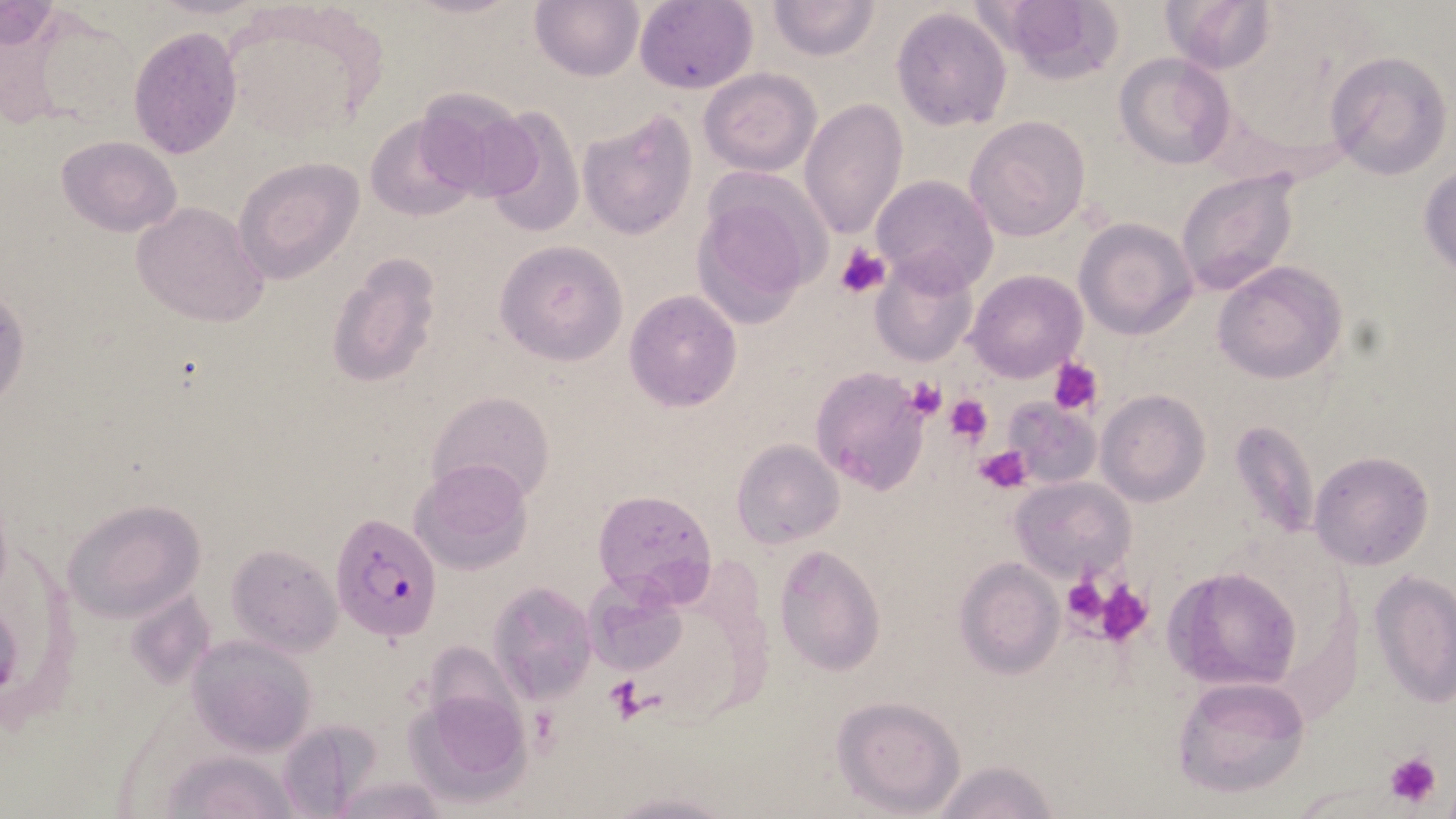
slide-level diagnosis = Plasmodium falciparum
stain = May-Grünwald-Giemsa
magnification = 1000x
modality = light microscopy
platelet locations = approximate bounding boxes as named x1/y1/x2/y2 corners in pixels: (x1=837, y1=247, x2=888, y2=298), (x1=1049, y1=357, x2=1105, y2=416), (x1=905, y1=378, x2=948, y2=421), (x1=946, y1=394, x2=993, y2=447), (x1=975, y1=445, x2=1029, y2=492), (x1=1061, y1=574, x2=1116, y2=635), (x1=1094, y1=578, x2=1154, y2=646), (x1=604, y1=676, x2=644, y2=722), (x1=528, y1=707, x2=559, y2=752), (x1=1382, y1=751, x2=1445, y2=811)
field of view = single
preparation = thin blood smear
image size = 1456×819 pixels
Plasmodium falciparum-infected red blood cell locations = approximate bounding boxes as named x1/y1/x2/y2 corners in pixels: (x1=333, y1=512, x2=441, y2=641)
uninfected red blood cell locations = approximate bounding boxes as named x1/y1/x2/y2 corners in pixels: (x1=531, y1=0, x2=645, y2=81), (x1=767, y1=0, x2=881, y2=60), (x1=980, y1=0, x2=1124, y2=82), (x1=1161, y1=0, x2=1277, y2=74), (x1=633, y1=1, x2=758, y2=93), (x1=1, y1=3, x2=60, y2=51), (x1=891, y1=6, x2=1013, y2=132), (x1=128, y1=25, x2=243, y2=160), (x1=1324, y1=51, x2=1453, y2=180), (x1=1114, y1=53, x2=1234, y2=168), (x1=699, y1=67, x2=821, y2=176), (x1=412, y1=86, x2=541, y2=202), (x1=799, y1=98, x2=908, y2=240), (x1=474, y1=105, x2=587, y2=235), (x1=578, y1=112, x2=697, y2=240), (x1=367, y1=114, x2=479, y2=222), (x1=965, y1=116, x2=1091, y2=241), (x1=56, y1=136, x2=183, y2=237), (x1=233, y1=157, x2=364, y2=283), (x1=1419, y1=163, x2=1455, y2=277), (x1=1175, y1=166, x2=1304, y2=300), (x1=870, y1=174, x2=998, y2=290), (x1=690, y1=176, x2=828, y2=323), (x1=131, y1=202, x2=269, y2=327), (x1=1074, y1=217, x2=1198, y2=338), (x1=495, y1=240, x2=627, y2=364), (x1=869, y1=252, x2=978, y2=367), (x1=326, y1=253, x2=442, y2=388), (x1=1212, y1=260, x2=1349, y2=386), (x1=965, y1=270, x2=1088, y2=383), (x1=623, y1=290, x2=743, y2=411), (x1=810, y1=367, x2=930, y2=494), (x1=1096, y1=390, x2=1211, y2=508), (x1=427, y1=391, x2=556, y2=505), (x1=1003, y1=399, x2=1101, y2=489), (x1=1228, y1=420, x2=1321, y2=546), (x1=732, y1=439, x2=844, y2=547), (x1=1307, y1=451, x2=1436, y2=572), (x1=410, y1=458, x2=533, y2=576), (x1=1010, y1=475, x2=1135, y2=583), (x1=591, y1=488, x2=719, y2=605), (x1=61, y1=499, x2=206, y2=625), (x1=225, y1=545, x2=340, y2=655), (x1=773, y1=545, x2=887, y2=678), (x1=955, y1=558, x2=1064, y2=678), (x1=1163, y1=567, x2=1301, y2=691), (x1=1369, y1=570, x2=1456, y2=708), (x1=581, y1=574, x2=689, y2=676), (x1=488, y1=580, x2=597, y2=703), (x1=187, y1=635, x2=318, y2=756), (x1=1171, y1=674, x2=1311, y2=798), (x1=405, y1=687, x2=532, y2=806), (x1=830, y1=694, x2=967, y2=817), (x1=274, y1=718, x2=382, y2=816), (x1=162, y1=750, x2=300, y2=819), (x1=927, y1=758, x2=1062, y2=819), (x1=329, y1=775, x2=449, y2=818), (x1=604, y1=790, x2=735, y2=819)